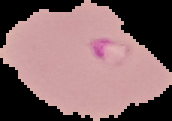
Image is 172×121 pixels. From a thin blood film. Cell region segmented out of the field of view; the surrounding area is masked to black. Malaria status: parasitized.